Report the malaria status of this cell.
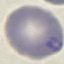

It is parasitized.

capture = smartphone camera at the microscope eyepiece
stain = Giemsa
image type = cell patch, automatically extracted from a larger field of view and resized to 64 × 64 pixels
preparation = thin blood film